Point out each Plasmodium parasite.
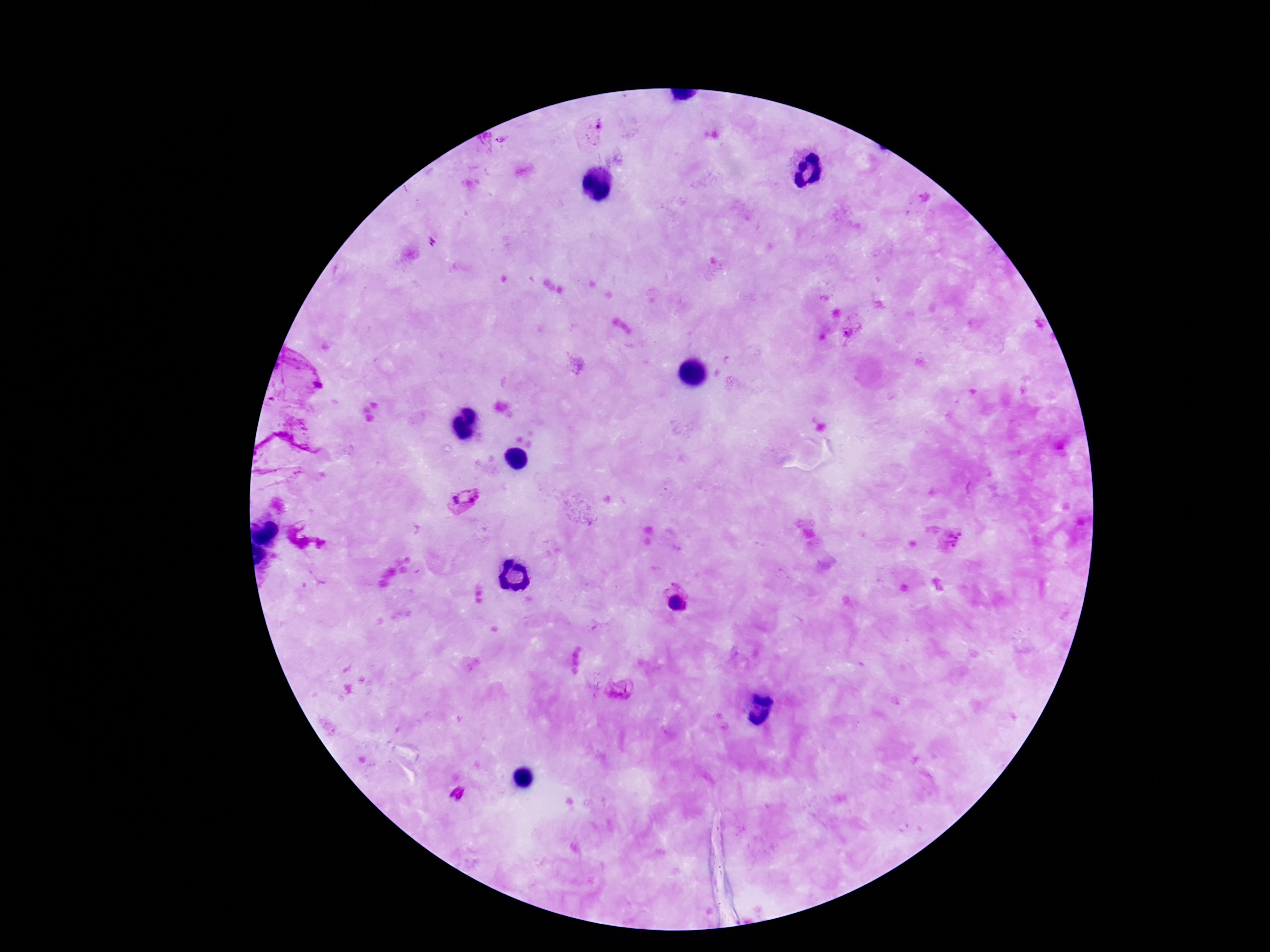

Approximate centers as (x, y) in pixels.
Plasmodium parasites: (594, 127), (501, 142), (433, 242), (853, 332), (466, 498), (951, 541), (677, 602), (620, 690).

{
  "patient_malaria_status": "positive",
  "magnification": "100x",
  "capture": "smartphone camera through the microscope eyepiece",
  "preparation": "thick blood film",
  "stain": "Giemsa",
  "image_size": "1270×952 pixels",
  "field_of_view": "single"
}